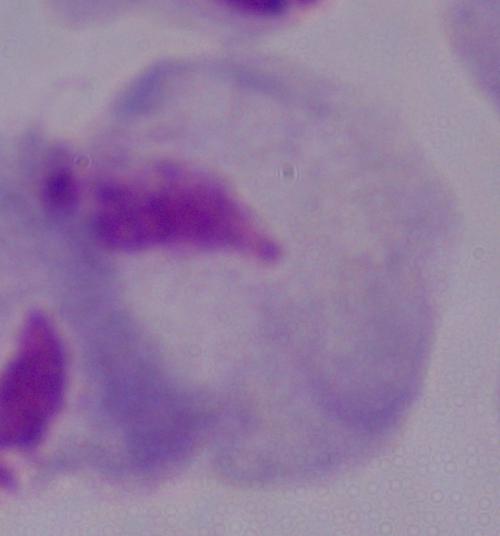
Summary:
  - Identification: trichomonad
  - Modality: micrograph
  - Magnification: 1000x